Identify the blood parasite species.
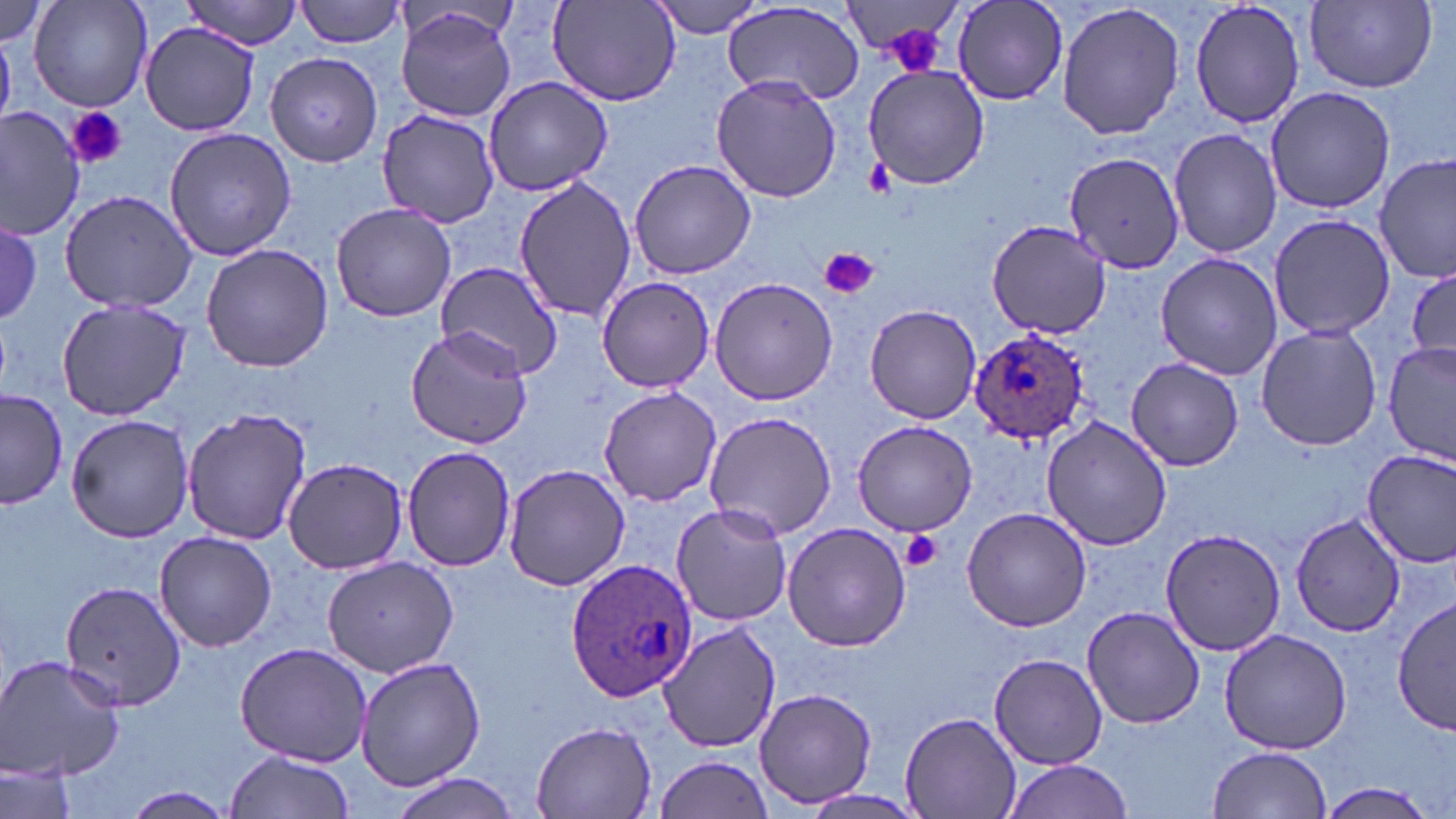

Plasmodium ovale.

Approximate bounding boxes as named x1/y1/x2/y2 corners in pixels. Uninfected red blood cell locations: (x1=30, y1=0, x2=154, y2=110), (x1=295, y1=0, x2=407, y2=49), (x1=953, y1=0, x2=1069, y2=105), (x1=1188, y1=0, x2=1308, y2=131), (x1=0, y1=1, x2=52, y2=48), (x1=182, y1=1, x2=304, y2=48), (x1=648, y1=1, x2=767, y2=39), (x1=724, y1=1, x2=864, y2=105), (x1=1057, y1=1, x2=1185, y2=140), (x1=1305, y1=1, x2=1437, y2=92), (x1=547, y1=2, x2=681, y2=108), (x1=842, y1=4, x2=961, y2=70), (x1=395, y1=7, x2=518, y2=122), (x1=138, y1=20, x2=264, y2=135), (x1=265, y1=52, x2=382, y2=166), (x1=861, y1=61, x2=992, y2=190), (x1=482, y1=75, x2=613, y2=196), (x1=711, y1=75, x2=843, y2=202), (x1=1264, y1=86, x2=1395, y2=213), (x1=0, y1=105, x2=85, y2=239), (x1=377, y1=108, x2=500, y2=228), (x1=163, y1=127, x2=296, y2=262), (x1=1169, y1=127, x2=1282, y2=258), (x1=1376, y1=150, x2=1454, y2=284), (x1=1063, y1=151, x2=1186, y2=276), (x1=627, y1=159, x2=759, y2=280), (x1=512, y1=174, x2=635, y2=323), (x1=61, y1=188, x2=197, y2=313), (x1=329, y1=202, x2=456, y2=321), (x1=1266, y1=212, x2=1398, y2=341), (x1=985, y1=219, x2=1111, y2=338), (x1=2, y1=220, x2=43, y2=326), (x1=200, y1=243, x2=334, y2=372), (x1=1155, y1=252, x2=1282, y2=380), (x1=435, y1=259, x2=564, y2=379), (x1=1405, y1=263, x2=1455, y2=369), (x1=597, y1=277, x2=716, y2=390), (x1=707, y1=277, x2=839, y2=405), (x1=56, y1=298, x2=192, y2=420), (x1=862, y1=304, x2=982, y2=426), (x1=1255, y1=324, x2=1384, y2=450), (x1=405, y1=326, x2=532, y2=450), (x1=1382, y1=342, x2=1454, y2=463), (x1=1127, y1=358, x2=1243, y2=472), (x1=598, y1=386, x2=723, y2=507), (x1=2, y1=388, x2=68, y2=511), (x1=181, y1=408, x2=312, y2=545), (x1=704, y1=412, x2=838, y2=540), (x1=65, y1=413, x2=196, y2=543), (x1=1041, y1=417, x2=1171, y2=550), (x1=850, y1=420, x2=979, y2=536), (x1=402, y1=446, x2=518, y2=572), (x1=1362, y1=452, x2=1456, y2=568), (x1=283, y1=457, x2=409, y2=573), (x1=502, y1=462, x2=632, y2=591), (x1=672, y1=503, x2=794, y2=626), (x1=961, y1=505, x2=1094, y2=632), (x1=1291, y1=513, x2=1406, y2=637), (x1=781, y1=521, x2=912, y2=652), (x1=1161, y1=528, x2=1285, y2=656), (x1=155, y1=532, x2=279, y2=652), (x1=321, y1=555, x2=458, y2=677), (x1=61, y1=581, x2=187, y2=714), (x1=1393, y1=596, x2=1455, y2=736), (x1=1082, y1=605, x2=1205, y2=729), (x1=658, y1=617, x2=782, y2=752), (x1=1217, y1=627, x2=1354, y2=756), (x1=234, y1=641, x2=373, y2=766), (x1=0, y1=652, x2=127, y2=784), (x1=989, y1=653, x2=1107, y2=768), (x1=355, y1=656, x2=487, y2=793), (x1=753, y1=687, x2=877, y2=807), (x1=898, y1=712, x2=1023, y2=819), (x1=530, y1=722, x2=660, y2=816), (x1=1208, y1=745, x2=1333, y2=819), (x1=224, y1=750, x2=358, y2=819), (x1=651, y1=755, x2=775, y2=819), (x1=999, y1=759, x2=1135, y2=819), (x1=2, y1=763, x2=79, y2=819), (x1=388, y1=773, x2=522, y2=818), (x1=1319, y1=781, x2=1440, y2=819), (x1=120, y1=786, x2=239, y2=819). Plasmodium ovale-infected red blood cell locations: (x1=969, y1=328, x2=1092, y2=441), (x1=565, y1=560, x2=697, y2=704). Platelet locations: (x1=877, y1=23, x2=955, y2=78), (x1=66, y1=104, x2=127, y2=171), (x1=867, y1=158, x2=895, y2=194), (x1=821, y1=247, x2=878, y2=299), (x1=901, y1=530, x2=944, y2=573). Captured at 1000x magnification. Image is 1456×819 pixels. Thin blood film. May-Grünwald-Giemsa stain. Optical microscopy. One field of a larger specimen.